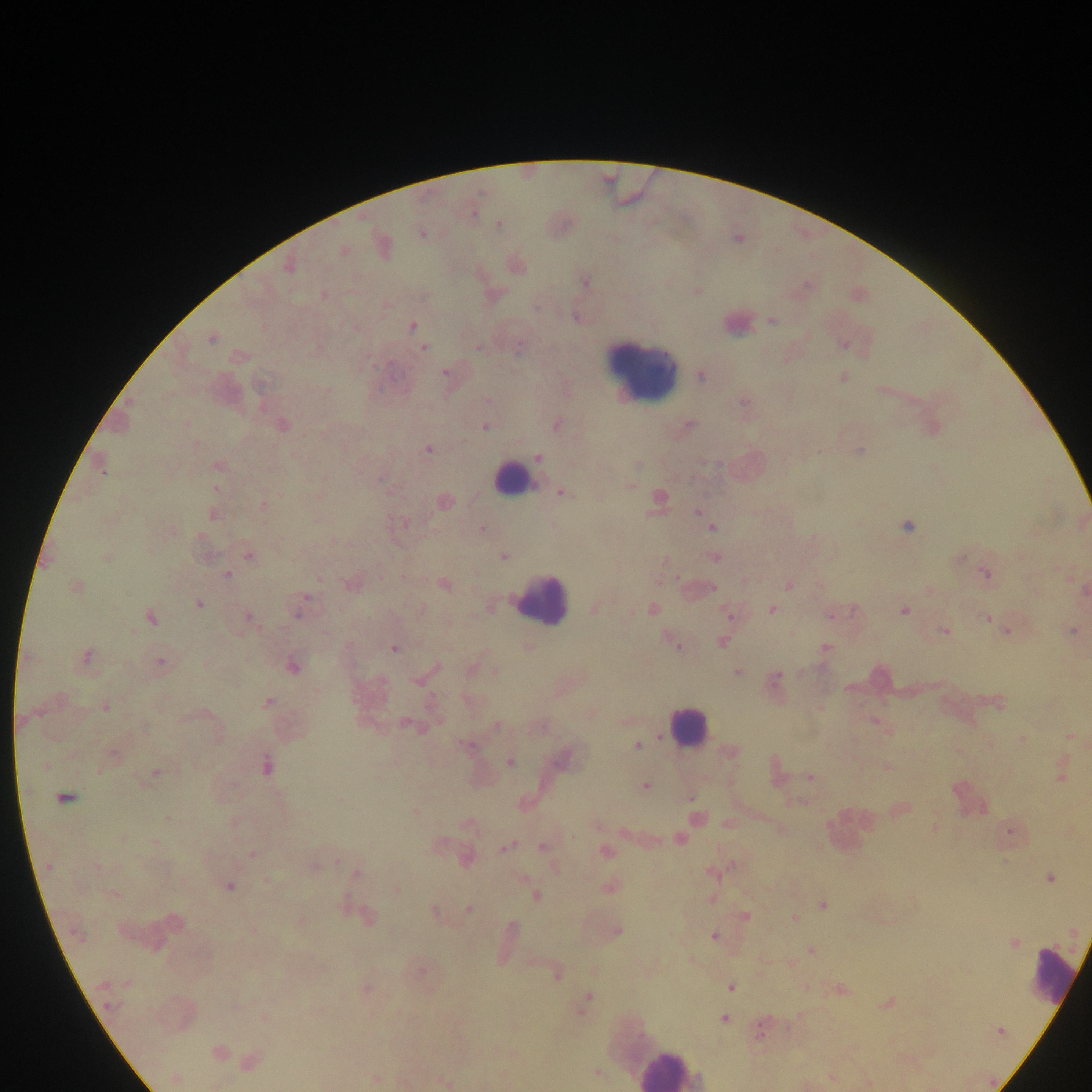

Approximate centers as (x, y) in pixels.
Summary:
  - Plasmodium parasite locations: (498, 224), (422, 233), (381, 243), (342, 250), (288, 265), (515, 265), (583, 282), (697, 290), (323, 294), (576, 318), (771, 320), (412, 325), (211, 338), (843, 344), (424, 347), (478, 347), (239, 356), (446, 372), (701, 376), (843, 378), (883, 390), (744, 402), (186, 423), (555, 424), (282, 425), (688, 425), (485, 426), (931, 428), (428, 449), (859, 451), (538, 458), (101, 466), (218, 466), (628, 485), (215, 488), (562, 492), (658, 499), (443, 502), (263, 505), (699, 512), (212, 514), (403, 523), (711, 526), (907, 526), (481, 529), (333, 541), (247, 555), (206, 556), (502, 556), (106, 557), (714, 557), (958, 557), (664, 560), (985, 574), (226, 575), (1069, 575), (661, 580), (351, 583), (444, 584), (788, 584), (75, 587), (930, 588), (696, 589), (1084, 590), (197, 603), (489, 604), (299, 607), (420, 608), (594, 609), (651, 609), (772, 609), (903, 611), (729, 614), (830, 614), (150, 616), (248, 617), (987, 618), (1073, 630), (944, 631), (1006, 631), (673, 641), (720, 642), (528, 646), (825, 647), (393, 648), (85, 656), (159, 661), (293, 665), (471, 669), (487, 670), (430, 671), (736, 671), (496, 672), (423, 676), (774, 679), (560, 688), (267, 702), (997, 702), (105, 706), (820, 707), (591, 712), (626, 720), (875, 721), (406, 724), (496, 726), (540, 726), (1070, 736), (1023, 740), (467, 744), (636, 746), (731, 752), (112, 755), (563, 757), (510, 762), (266, 765), (888, 767), (1061, 771), (155, 773), (775, 773), (810, 777), (644, 786), (64, 797), (691, 798), (899, 809), (415, 811), (696, 817), (169, 819), (235, 822), (468, 823), (727, 824), (596, 826), (934, 827), (1009, 830), (121, 837), (679, 838), (153, 843), (542, 846), (506, 847), (605, 851), (252, 854), (463, 856), (314, 865), (49, 866), (711, 871), (355, 874), (1049, 877), (228, 886), (609, 886), (396, 889), (114, 894), (535, 896), (710, 898), (823, 904), (468, 910), (435, 912), (745, 916), (366, 917), (794, 918), (300, 920), (173, 922), (616, 931), (714, 937), (1013, 943), (811, 951), (690, 960), (790, 964), (419, 971), (557, 973), (730, 986), (365, 989), (840, 990), (585, 1002), (887, 1002), (265, 1018), (724, 1018), (761, 1028), (999, 1031), (217, 1053), (249, 1061), (595, 1072), (175, 1077), (831, 1077), (374, 1079), (444, 1081), (866, 1084)
  - Leukocyte locations: (737, 321), (641, 367), (513, 479), (540, 598), (687, 727), (848, 830), (1052, 978), (668, 1067)
  - Field of view: single
  - Capture: mobile-phone photograph through a microscope
  - Country: Ghana
  - Preparation: thick blood smear
  - Image size: 1092×1092 pixels